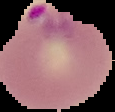

Summary:
  - Image size: 115×112 pixels
  - Malaria status: parasitized
  - Image type: cell region segmented out of the field of view; surrounding area masked to black
  - Preparation: thin blood smear